Give the position of every Plasmodium parasite visible.
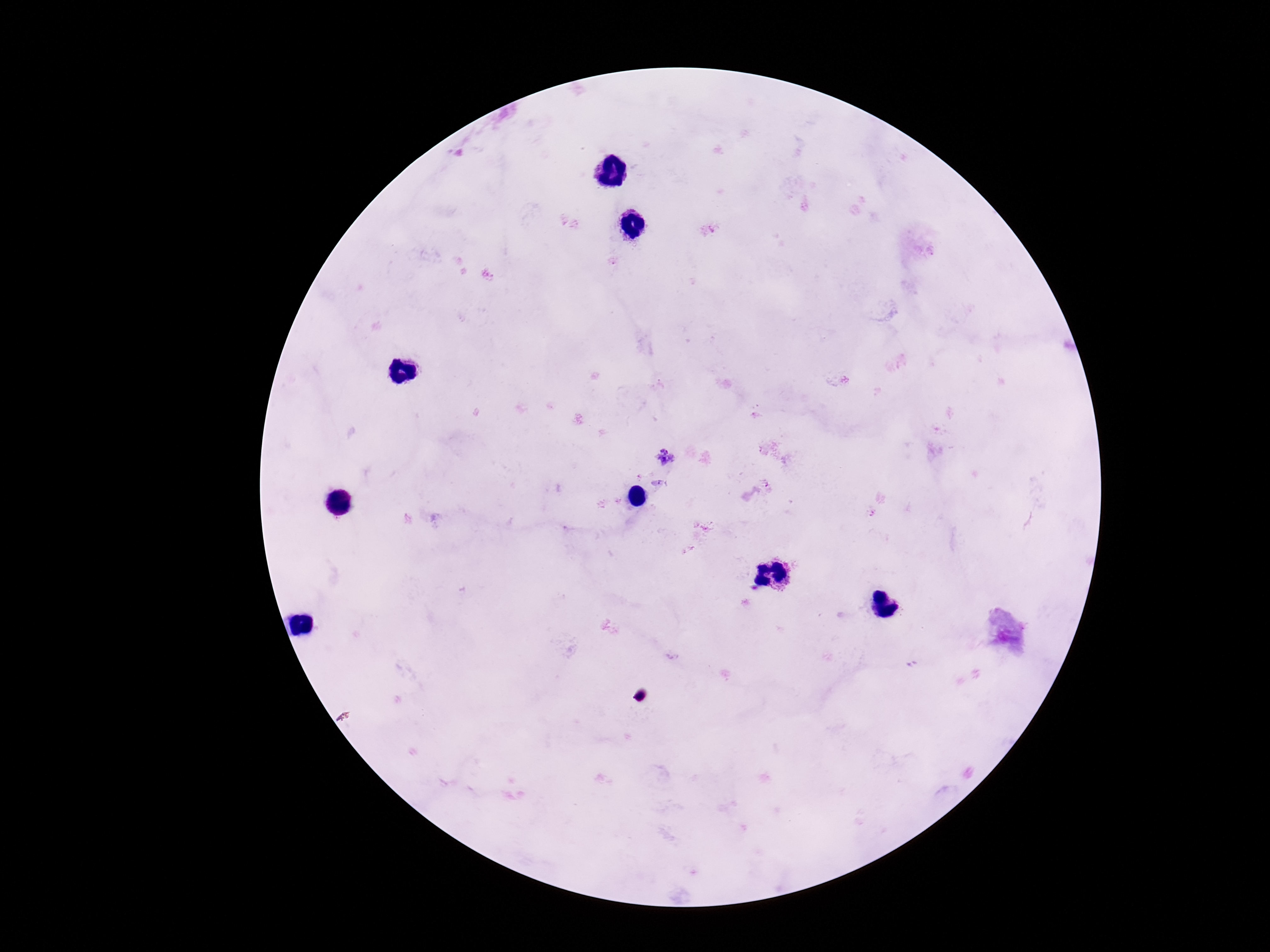

Approximate centers as [x, y] in pixels.
Plasmodium parasites: [665, 457], [663, 482], [765, 484].

Image is 1270×952 pixels. Single field of view. Thick peripheral-blood smear. Patient malaria status: infected. 100x magnification. Photographed through the microscope eyepiece with a smartphone camera. Giemsa stain.